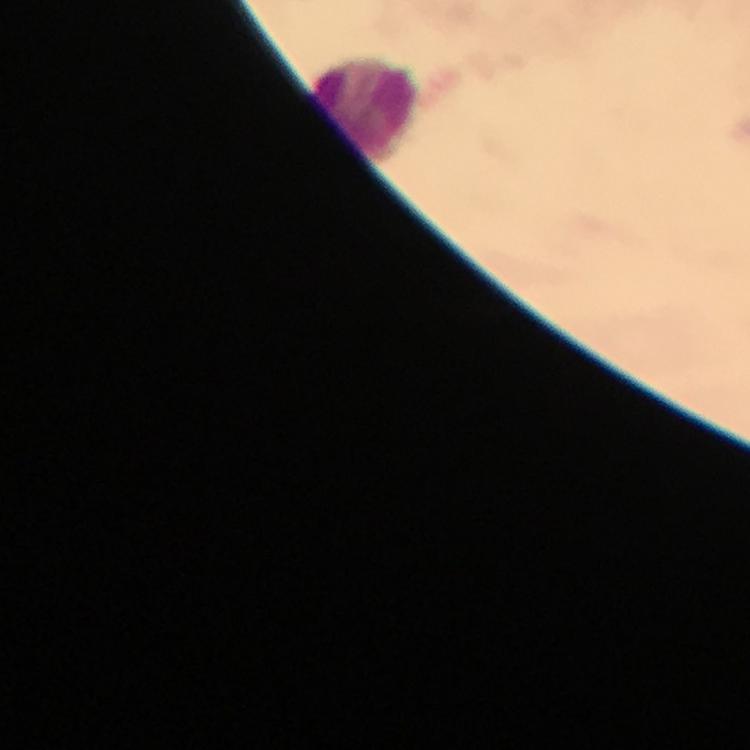

Approximate object centers, in pixels from the top-left corner.
Summary:
  - Leukocyte locations: (x=366, y=106)
  - Capture: smartphone mounted on the microscope
  - Image size: 750×750 pixels
  - Preparation: thick blood film
  - Cropped from: one field of view
  - Immersion oil: used
  - Magnification: 100x
  - Context: from a malaria diagnostic workup
  - Stain: Giemsa
  - Malaria parasites: none seen